Outline each blood parasite and name the species.
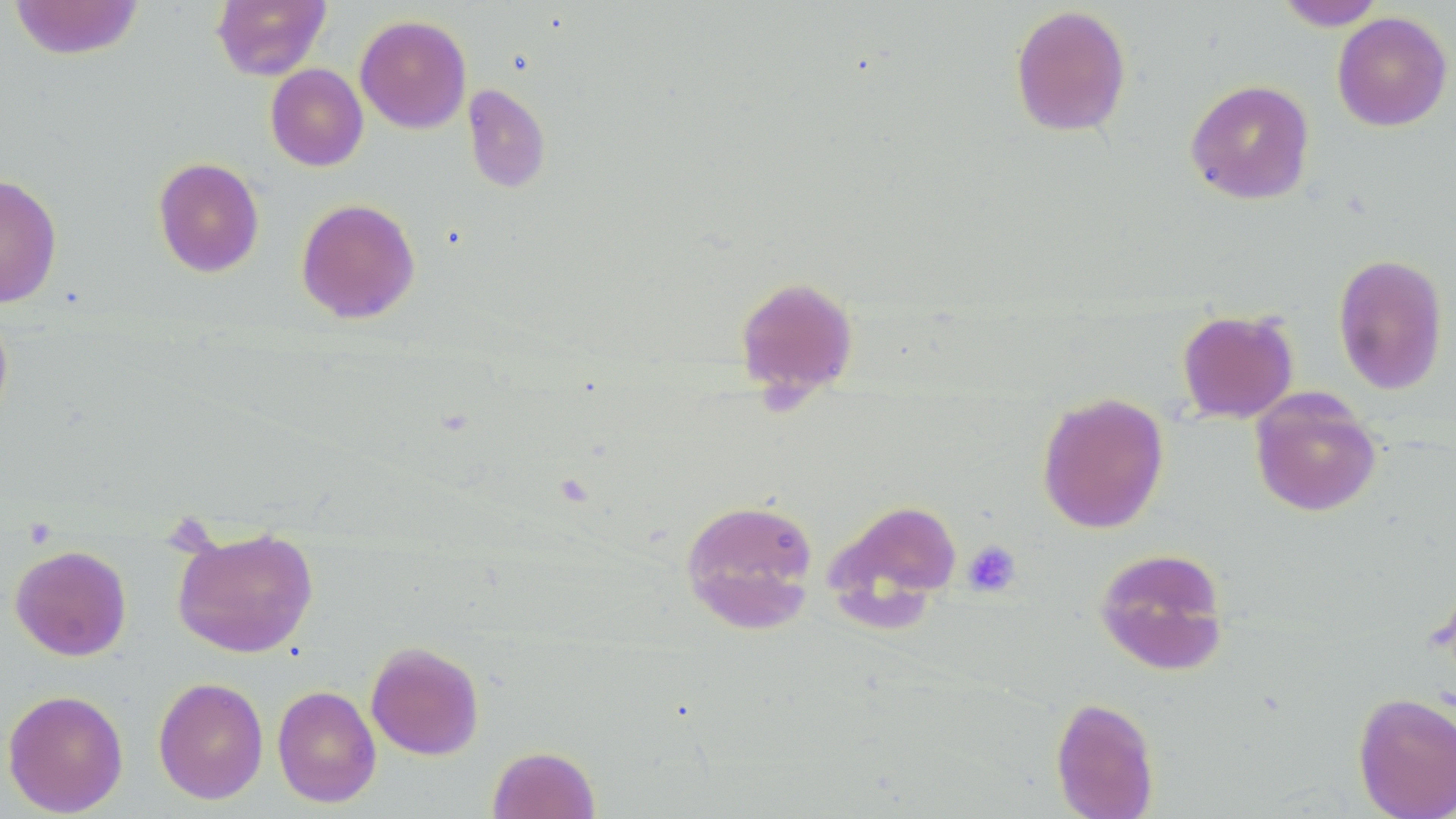

No blood parasites observed.

Approximate bounding boxes as [x1, y1, x2, y2] in pixels. Uninfected red blood cell locations: [7, 0, 146, 60], [211, 0, 331, 81], [1274, 0, 1387, 30], [1009, 4, 1132, 138], [1332, 12, 1453, 132], [355, 14, 472, 134], [265, 64, 368, 172], [1185, 79, 1315, 205], [462, 83, 551, 194], [153, 157, 265, 278], [0, 173, 63, 308], [296, 197, 421, 324], [1332, 252, 1449, 396], [733, 275, 859, 401], [0, 306, 14, 432], [1176, 308, 1299, 423], [1250, 389, 1383, 518], [1036, 391, 1170, 534], [680, 497, 820, 632], [823, 498, 963, 630], [172, 525, 319, 659], [10, 544, 131, 661], [1093, 546, 1231, 675], [365, 640, 485, 760], [153, 676, 269, 805], [272, 684, 381, 808], [2, 689, 129, 816], [1351, 691, 1456, 818], [1050, 696, 1161, 819], [487, 745, 600, 819]. Platelet locations: [962, 540, 1021, 597]. Slide-level diagnosis: no evidence of blood parasites. 1000x magnification. Thin blood smear. Light microscopy. One field of a larger specimen. Image is 1456×819 pixels. May-Grünwald-Giemsa stain.